Identify the parasite.
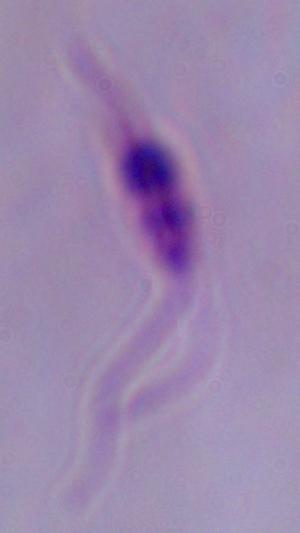

Leishmania.

{
  "magnification": "1000x",
  "modality": "micrograph"
}